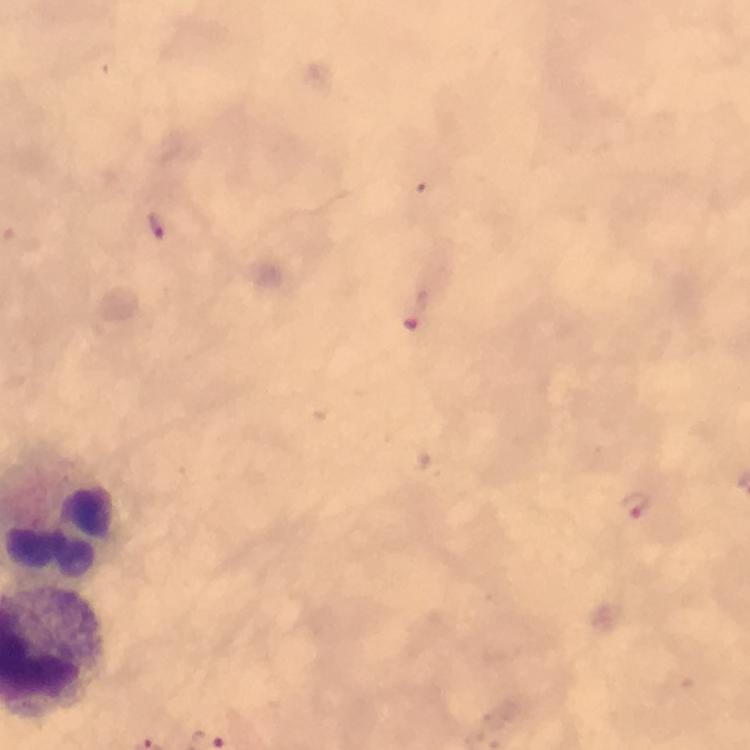 Approximate centers as (x, y) in pixels. Plasmodium parasite locations: (158, 227), (414, 320), (637, 506). Image is 750×750 pixels. 100x magnification. Thick smear. From a diagnostic examination for malaria. Giemsa-stained preparation. Cropped region of a single field of view. Smartphone photograph taken through a microscope. Immersion oil applied.